Name the parasite shown.
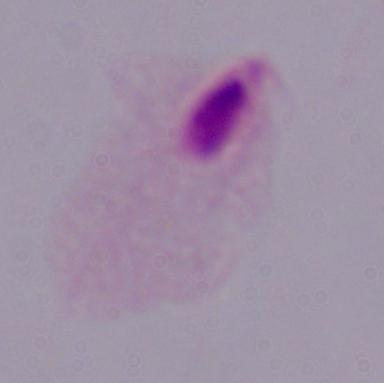

This is a trichomonad.

magnification = 1000x
modality = photomicrograph